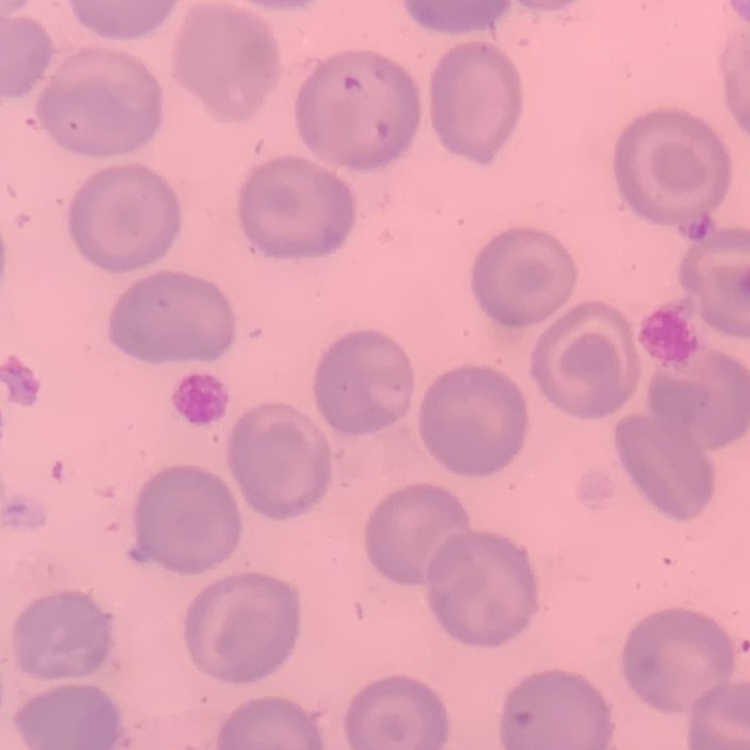

The erythrocytes exhibit no rouleaux formation. Square crop of a larger photomicrograph. Thin blood film. Field's or Giemsa stain.